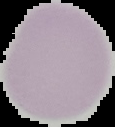
Summary:
  - Image type: cell region segmented out of the field of view; surrounding area masked to black
  - Malaria status: uninfected
  - Image size: 115×127 pixels
  - Preparation: thin blood smear